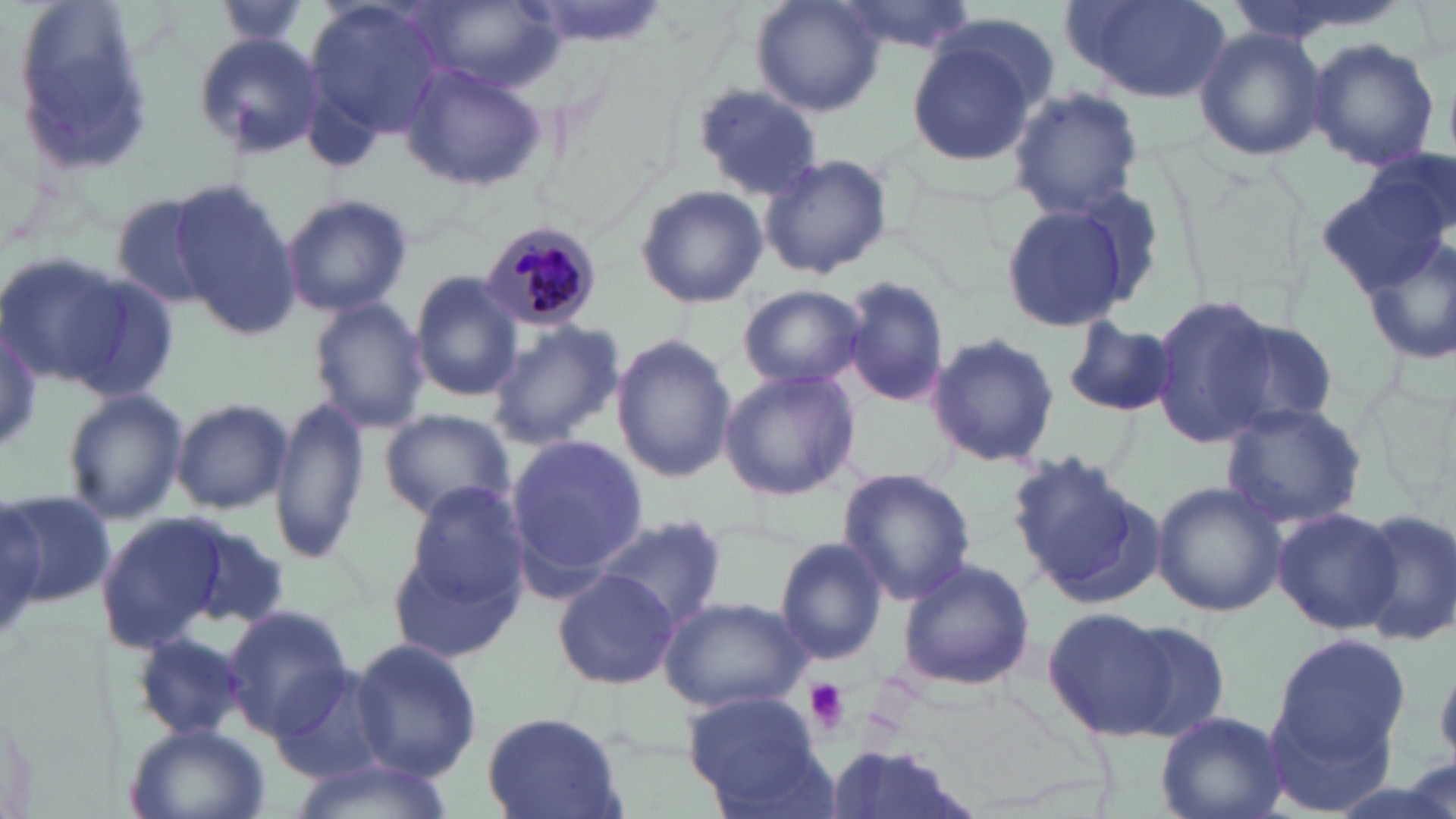
slide_level_diagnosis: Plasmodium malariae
platelet_locations: 'approximate bounding boxes as [x1, y1, x2, y2] in pixels: [801, 679, 850, 735]'
plasmodium_malariae_infected_red_blood_cell_locations: 'approximate bounding boxes as [x1, y1, x2, y2] in pixels: [479, 220, 605, 334]'
stain: May-Grünwald-Giemsa
magnification: 1000x
image_size: 1456×819 pixels
field_of_view: single
uninfected_red_blood_cell_locations: 'approximate bounding boxes as [x1, y1, x2, y2] in pixels: [211, 0, 316, 48], [750, 0, 887, 115], [305, 1, 450, 142], [831, 1, 977, 57], [1066, 1, 1229, 103], [11, 2, 153, 180], [413, 2, 562, 96], [1193, 26, 1326, 162], [905, 29, 1044, 169], [191, 31, 327, 159], [1307, 38, 1439, 171], [401, 63, 546, 191], [694, 82, 824, 201], [1005, 87, 1146, 215], [1326, 145, 1453, 339], [759, 153, 894, 282], [168, 180, 301, 336], [635, 185, 768, 309], [108, 191, 228, 310], [281, 193, 413, 318], [999, 202, 1133, 333], [0, 251, 133, 391], [52, 270, 183, 406], [409, 270, 524, 402], [841, 278, 949, 405], [736, 283, 867, 390], [1148, 294, 1280, 448], [308, 298, 430, 433], [1063, 317, 1178, 417], [485, 319, 625, 448], [1220, 320, 1340, 431], [0, 326, 46, 453], [923, 331, 1058, 467], [611, 335, 736, 482], [718, 367, 863, 501], [62, 387, 187, 526], [169, 396, 293, 514], [270, 396, 371, 561], [1220, 402, 1368, 532], [378, 410, 516, 522], [505, 431, 649, 586], [1009, 451, 1160, 602], [836, 467, 975, 604], [1150, 480, 1286, 617], [401, 481, 531, 613], [2, 490, 117, 607], [0, 496, 45, 645], [1272, 506, 1400, 633], [1350, 508, 1456, 648], [95, 513, 230, 652], [589, 513, 728, 632], [170, 514, 290, 631], [387, 524, 528, 669], [773, 537, 888, 667], [898, 558, 1034, 690], [552, 569, 678, 689], [658, 595, 813, 714], [220, 604, 355, 741], [1042, 607, 1178, 742], [1116, 617, 1232, 738], [132, 630, 252, 742], [1268, 634, 1413, 774], [348, 638, 482, 779], [272, 662, 399, 785], [684, 693, 830, 812], [1158, 709, 1290, 819], [479, 713, 629, 819], [125, 721, 271, 819], [817, 745, 986, 819], [282, 754, 455, 819]'
preparation: thin blood film
modality: light microscopy